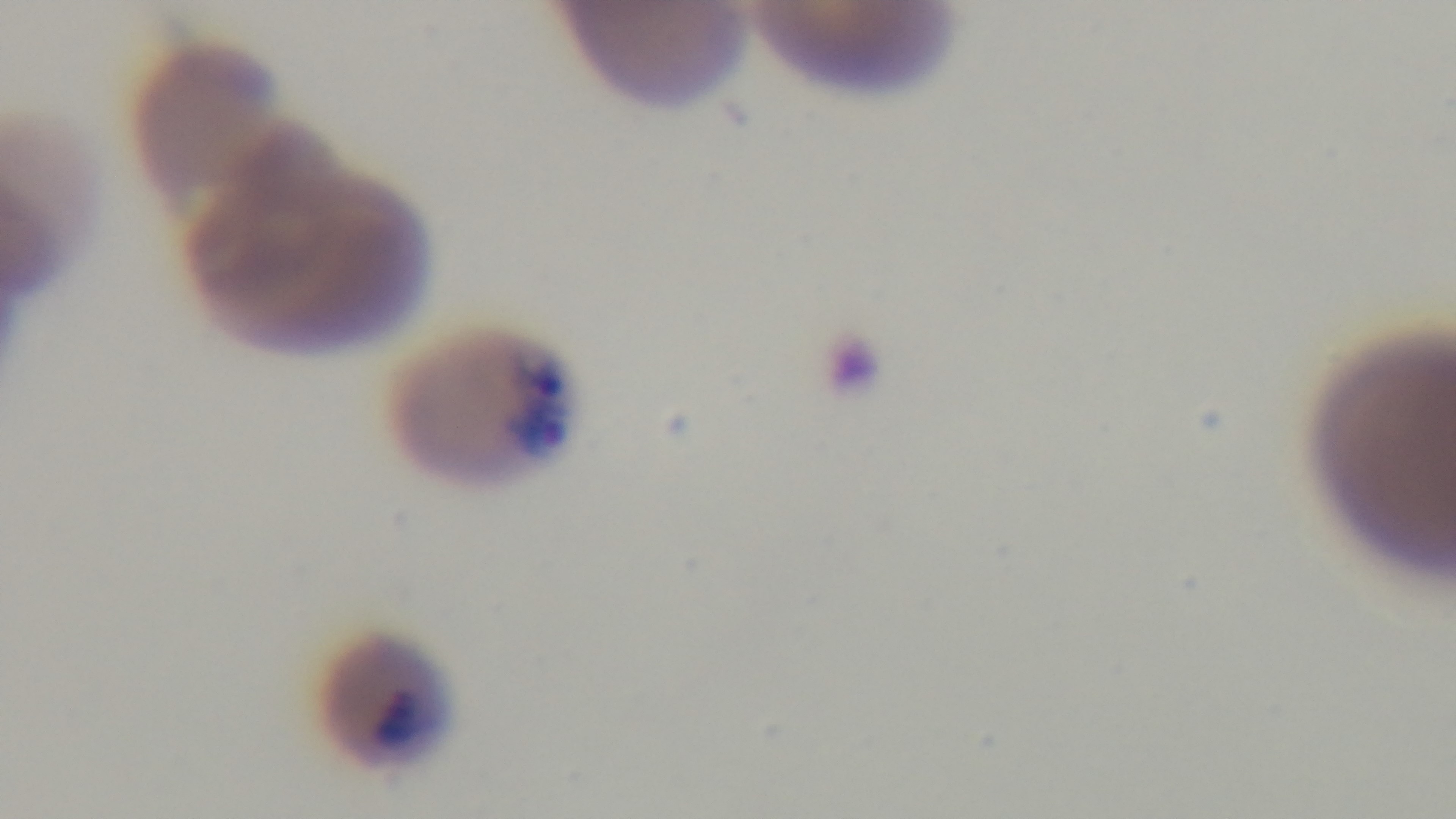
field of view = one from the slide
malaria status = infected
capture = mounted 4K digital camera
preparation = thin smear
stain = Giemsa
objective = 100x oil immersion
modality = light microscopy